Locate every malaria parasite.
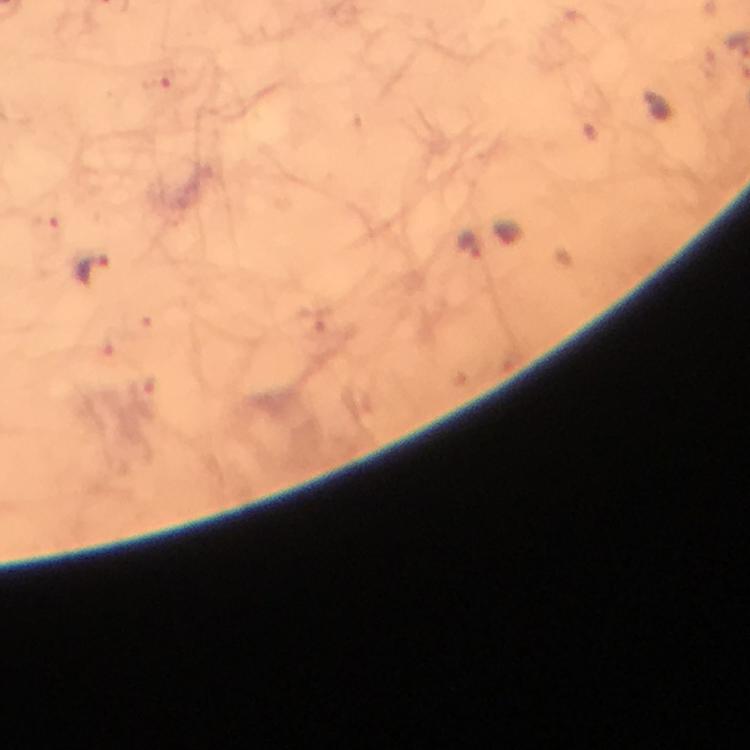
Approximate centers as {x, y} in pixels.
Malaria parasites: {154, 83}, {46, 232}, {469, 244}, {93, 270}.

Giemsa-stained preparation. From a malaria diagnostic workup. Immersion oil applied. Image is 750×750 pixels. At 100x magnification. Smartphone photograph taken through a microscope. Cropped region of a single field of view. Thick smear.